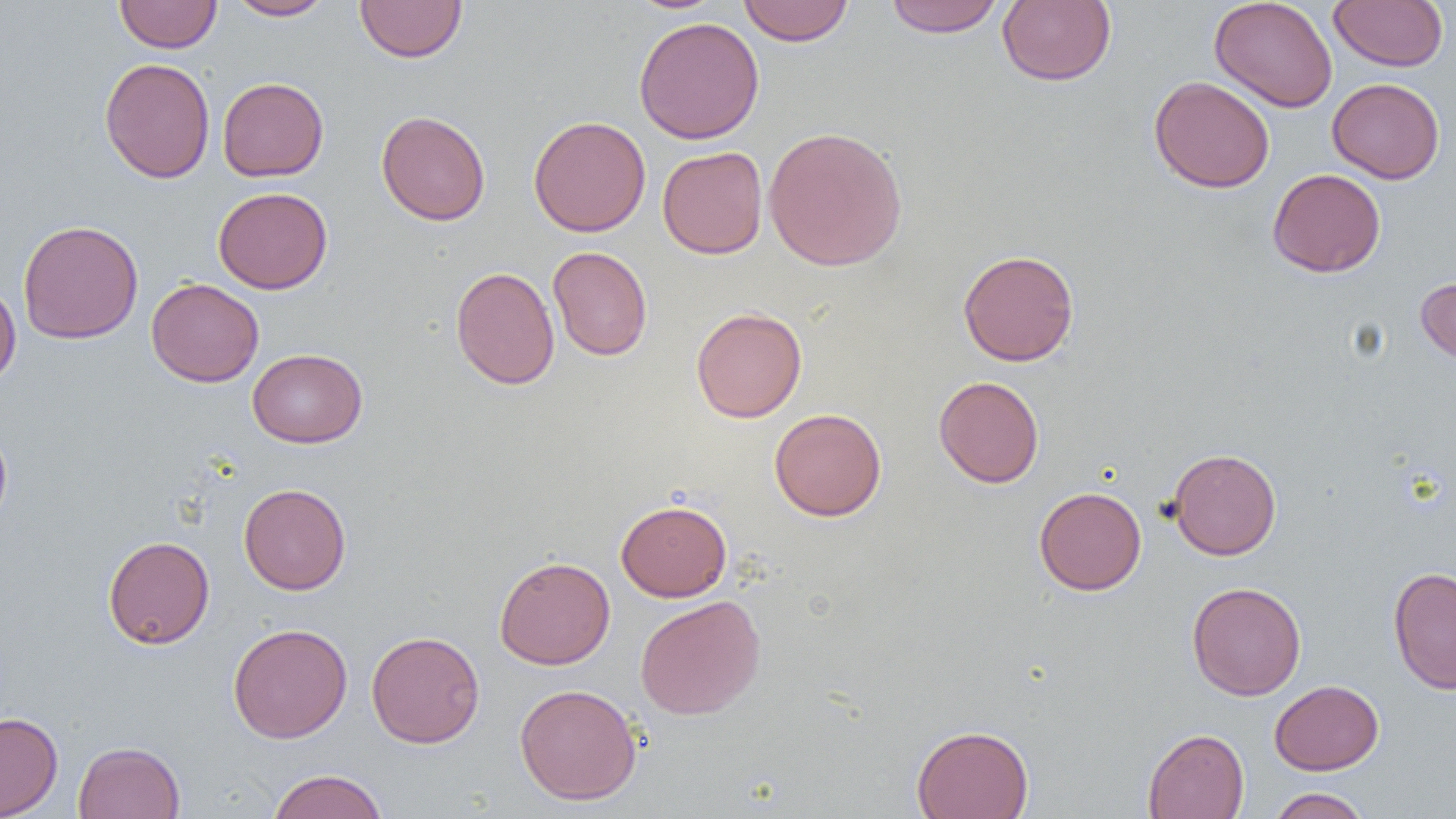

Approximate bounding boxes as [x1, y1, x2, y2] in pixels. Uninfected red blood cell locations: [114, 0, 222, 53], [225, 0, 335, 20], [355, 0, 468, 63], [738, 0, 854, 46], [883, 0, 1005, 37], [997, 0, 1116, 86], [1209, 0, 1338, 113], [1328, 0, 1449, 72], [633, 16, 765, 144], [98, 57, 215, 183], [1149, 76, 1275, 193], [217, 77, 329, 181], [1327, 78, 1445, 183], [376, 110, 491, 226], [528, 115, 651, 237], [763, 126, 908, 271], [657, 146, 768, 259], [1268, 168, 1386, 277], [213, 186, 332, 294], [17, 219, 144, 344], [548, 246, 653, 361], [958, 249, 1079, 366], [450, 266, 560, 390], [1416, 276, 1456, 366], [146, 278, 264, 387], [0, 281, 21, 389], [691, 307, 807, 422], [247, 348, 367, 447], [933, 376, 1044, 488], [769, 408, 886, 521], [0, 424, 12, 534], [1167, 448, 1282, 560], [238, 483, 351, 595], [1033, 486, 1146, 595], [616, 499, 731, 602], [102, 535, 215, 649], [494, 556, 615, 669], [1388, 566, 1456, 694], [1186, 581, 1306, 700], [635, 595, 766, 720], [228, 623, 353, 743], [366, 630, 485, 748], [1269, 680, 1384, 775], [514, 683, 642, 805], [0, 712, 63, 818], [911, 724, 1034, 819], [1142, 728, 1249, 819], [73, 741, 185, 819], [267, 769, 388, 819], [1267, 787, 1371, 819]. Slide-level diagnosis: negative for blood parasites. One field of a larger specimen. Optical microscopy. Captured at 1000x magnification. Thin blood smear. Image is 1456×819 pixels.